Assess the morphology of the erythrocytes.
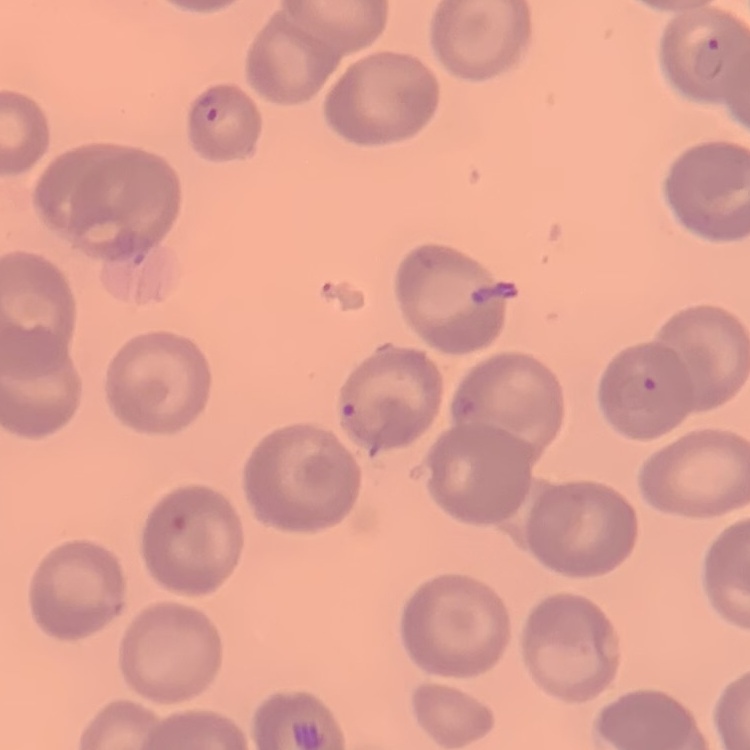

No rouleaux formation.

Field's or Giemsa stain. Square crop of a larger photomicrograph. Thin peripheral smear.